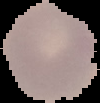
Summary:
  - Malaria status: parasitized
  - Image type: segmented cell region on a black background
  - Preparation: thin blood smear
  - Image size: 100×103 pixels